State which parasite is depicted.
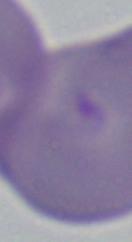
This is Babesia.

Summary:
  - Magnification: 1000x
  - Modality: micrograph